Mark where platelets are.
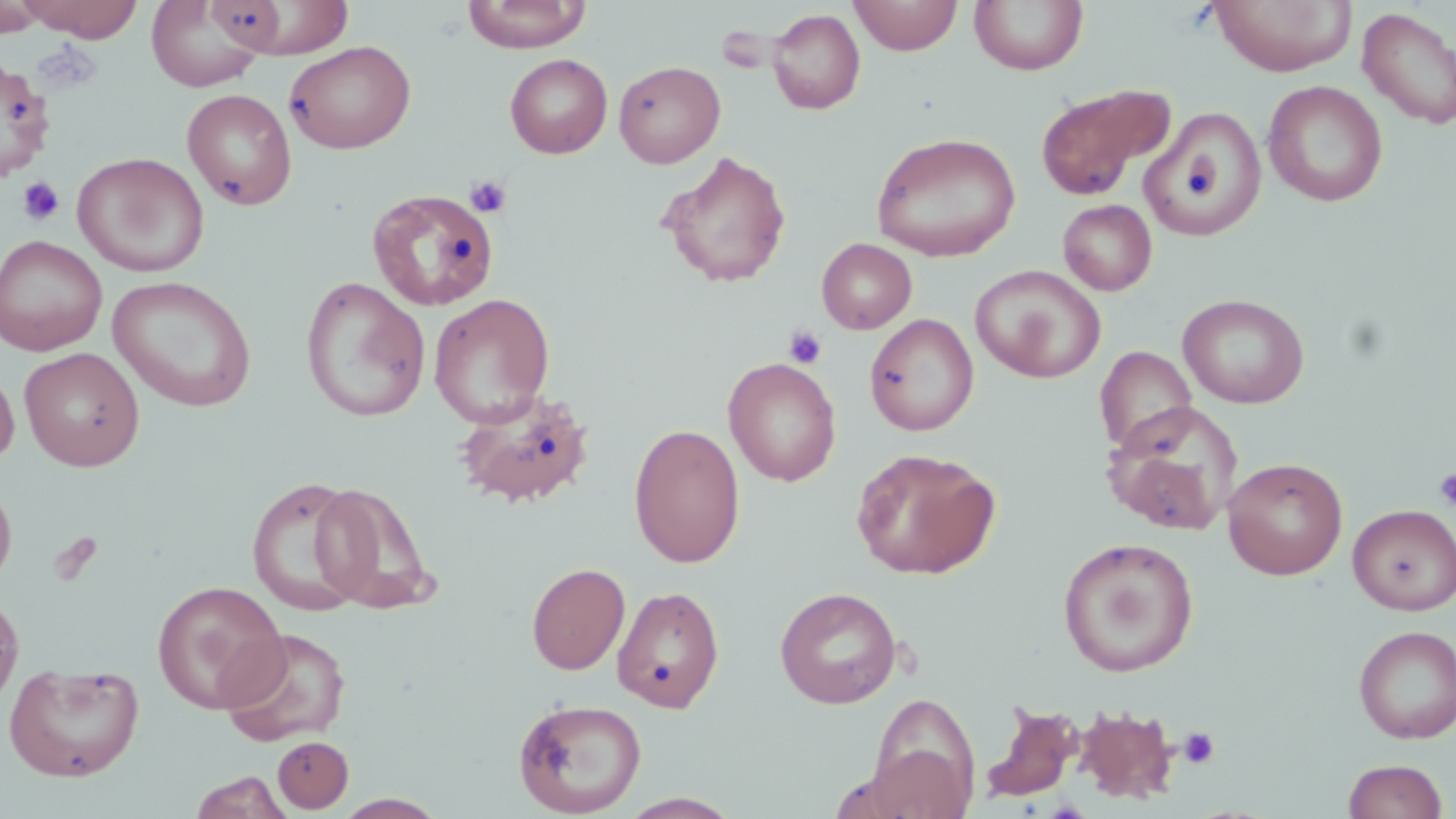
Approximate bounding boxes as [x1, y1, x2, y2] in pixels.
Platelets: [465, 175, 512, 219], [18, 176, 64, 225], [784, 326, 827, 368], [1433, 467, 1456, 510], [1178, 727, 1221, 769].

slide_level_diagnosis: negative for blood parasites
stain: May-Grünwald-Giemsa
uninfected_red_blood_cell_locations: 'approximate bounding boxes as [x1, y1, x2, y2] in pixels: [18, 0, 144, 41], [219, 0, 355, 59], [462, 0, 591, 53], [849, 0, 963, 55], [969, 0, 1088, 76], [1209, 0, 1357, 76], [0, 1, 47, 37], [147, 1, 265, 91], [1357, 7, 1456, 130], [767, 8, 866, 114], [283, 40, 416, 154], [505, 53, 612, 158], [0, 57, 55, 183], [613, 60, 725, 168], [1262, 80, 1388, 207], [1035, 84, 1175, 200], [182, 88, 297, 210], [1141, 107, 1267, 240], [871, 131, 1021, 262], [72, 151, 210, 277], [659, 151, 792, 288], [367, 188, 498, 312], [1058, 199, 1157, 296], [0, 234, 107, 356], [817, 238, 917, 334], [970, 264, 1106, 383], [107, 276, 257, 412], [299, 276, 431, 423], [428, 293, 555, 428], [1178, 293, 1309, 409], [864, 313, 979, 436], [1094, 346, 1197, 455], [20, 347, 144, 471], [723, 357, 842, 486], [0, 362, 19, 467], [453, 388, 596, 508], [1103, 402, 1243, 535], [628, 422, 746, 568], [850, 446, 1001, 580], [1223, 457, 1348, 580], [0, 475, 17, 592], [247, 476, 368, 617], [309, 482, 435, 615], [1348, 504, 1456, 615], [1058, 537, 1199, 677], [526, 562, 630, 675], [152, 580, 287, 714], [612, 585, 725, 713], [774, 587, 901, 708], [0, 593, 24, 713], [1354, 625, 1456, 743], [218, 626, 351, 748], [4, 661, 144, 782], [866, 692, 982, 817], [513, 698, 647, 817], [978, 701, 1085, 803], [1072, 704, 1180, 805], [273, 736, 354, 813], [1342, 758, 1448, 819], [188, 771, 295, 819], [617, 792, 743, 818], [332, 793, 449, 818]'
preparation: thin blood smear
field_of_view: single
image_size: 1456×819 pixels
magnification: 1000x
modality: optical microscopy